Locate every Plasmodium falciparum-infected red blood cell.
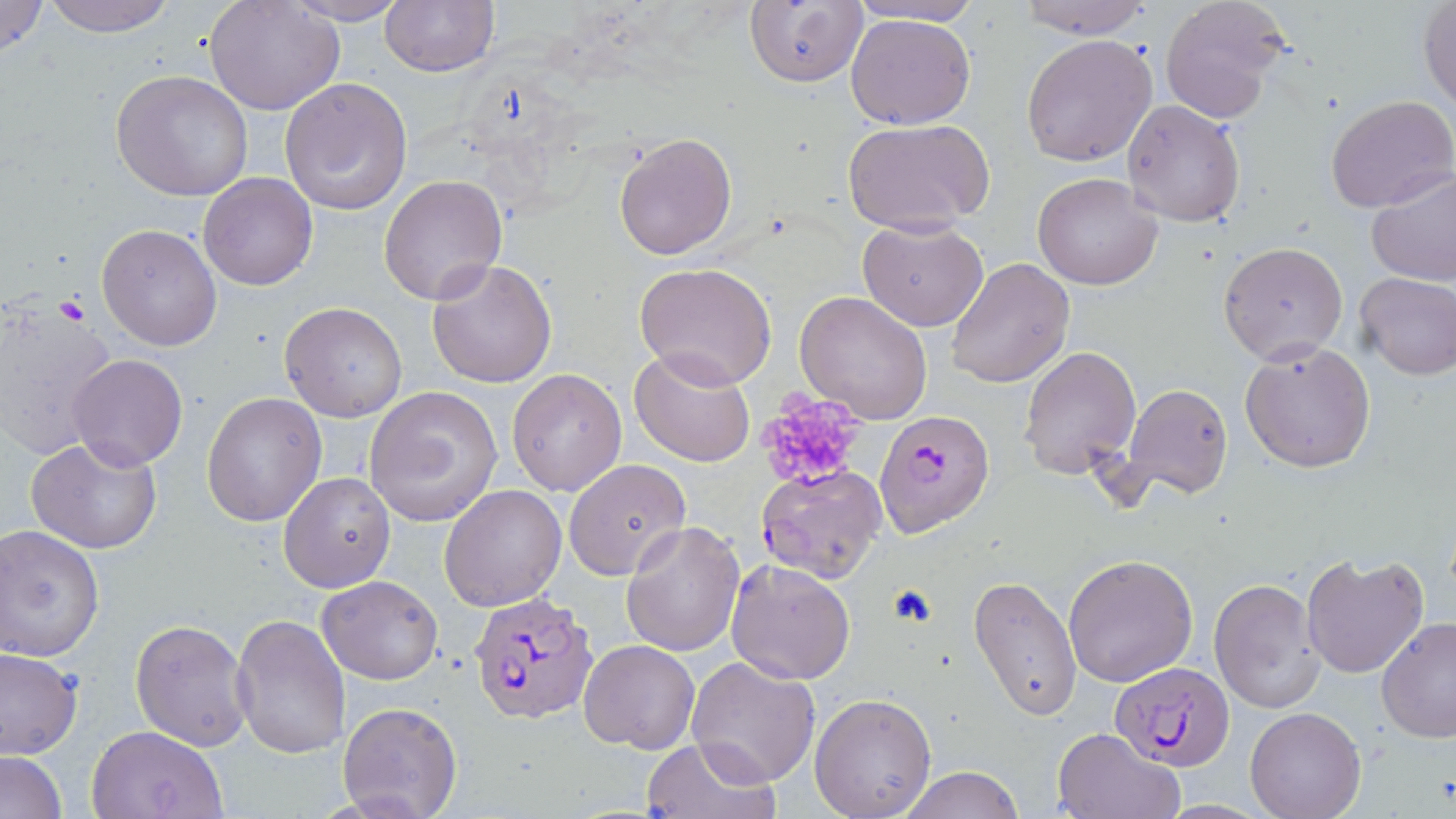
Approximate bounding boxes as named x1/y1/x2/y2 corners in pixels.
Plasmodium falciparum-infected red blood cells: (x1=875, y1=409, x2=995, y2=537), (x1=758, y1=466, x2=888, y2=585), (x1=467, y1=594, x2=599, y2=723), (x1=1112, y1=663, x2=1234, y2=768).

slide_level_diagnosis: Plasmodium falciparum
magnification: 1000x
preparation: thin blood film
stain: May-Grünwald-Giemsa
image_size: 1456×819 pixels
uninfected_red_blood_cell_locations: 'approximate bounding boxes as named x1/y1/x2/y2 corners in pixels: (x1=0, y1=0, x2=50, y2=60), (x1=38, y1=0, x2=180, y2=36), (x1=379, y1=0, x2=500, y2=75), (x1=842, y1=0, x2=989, y2=27), (x1=1012, y1=0, x2=1156, y2=37), (x1=1158, y1=0, x2=1293, y2=124), (x1=205, y1=1, x2=345, y2=117), (x1=282, y1=1, x2=413, y2=25), (x1=743, y1=1, x2=869, y2=88), (x1=1417, y1=2, x2=1456, y2=114), (x1=846, y1=12, x2=977, y2=129), (x1=1021, y1=35, x2=1158, y2=167), (x1=111, y1=70, x2=254, y2=200), (x1=279, y1=75, x2=414, y2=216), (x1=1326, y1=95, x2=1456, y2=213), (x1=1121, y1=99, x2=1247, y2=227), (x1=842, y1=118, x2=994, y2=235), (x1=613, y1=131, x2=738, y2=260), (x1=1365, y1=167, x2=1456, y2=287), (x1=198, y1=172, x2=318, y2=291), (x1=1032, y1=173, x2=1163, y2=291), (x1=378, y1=174, x2=509, y2=306), (x1=856, y1=217, x2=989, y2=332), (x1=96, y1=223, x2=222, y2=352), (x1=891, y1=230, x2=1037, y2=366), (x1=1218, y1=243, x2=1348, y2=364), (x1=427, y1=258, x2=558, y2=389), (x1=947, y1=258, x2=1075, y2=388), (x1=636, y1=263, x2=776, y2=390), (x1=1355, y1=270, x2=1455, y2=379), (x1=794, y1=292, x2=933, y2=426), (x1=1, y1=300, x2=121, y2=462), (x1=280, y1=302, x2=407, y2=422), (x1=1240, y1=339, x2=1376, y2=475), (x1=1018, y1=345, x2=1142, y2=481), (x1=629, y1=346, x2=756, y2=466), (x1=67, y1=353, x2=187, y2=469), (x1=507, y1=369, x2=628, y2=496), (x1=1121, y1=382, x2=1233, y2=498), (x1=363, y1=386, x2=504, y2=527), (x1=201, y1=391, x2=326, y2=526), (x1=27, y1=436, x2=165, y2=553), (x1=562, y1=457, x2=691, y2=580), (x1=278, y1=472, x2=396, y2=592), (x1=439, y1=484, x2=567, y2=611), (x1=620, y1=520, x2=746, y2=656), (x1=1, y1=525, x2=104, y2=661), (x1=1301, y1=551, x2=1430, y2=679), (x1=1063, y1=554, x2=1198, y2=686), (x1=725, y1=560, x2=857, y2=684), (x1=317, y1=575, x2=443, y2=684), (x1=970, y1=575, x2=1082, y2=720), (x1=1208, y1=578, x2=1324, y2=714), (x1=228, y1=613, x2=352, y2=760), (x1=1376, y1=616, x2=1456, y2=742), (x1=130, y1=619, x2=253, y2=752), (x1=578, y1=640, x2=700, y2=754), (x1=1, y1=648, x2=82, y2=759), (x1=686, y1=657, x2=821, y2=790), (x1=810, y1=693, x2=937, y2=818), (x1=337, y1=700, x2=462, y2=819), (x1=1245, y1=707, x2=1366, y2=818), (x1=87, y1=724, x2=229, y2=818), (x1=1052, y1=726, x2=1184, y2=818), (x1=641, y1=737, x2=778, y2=819), (x1=1, y1=751, x2=67, y2=819), (x1=896, y1=766, x2=1025, y2=819)'
platelet_locations: 'approximate bounding boxes as named x1/y1/x2/y2 corners in pixels: (x1=755, y1=391, x2=869, y2=494), (x1=887, y1=583, x2=939, y2=627)'
field_of_view: single
modality: optical microscopy